Outline every malaria parasite.
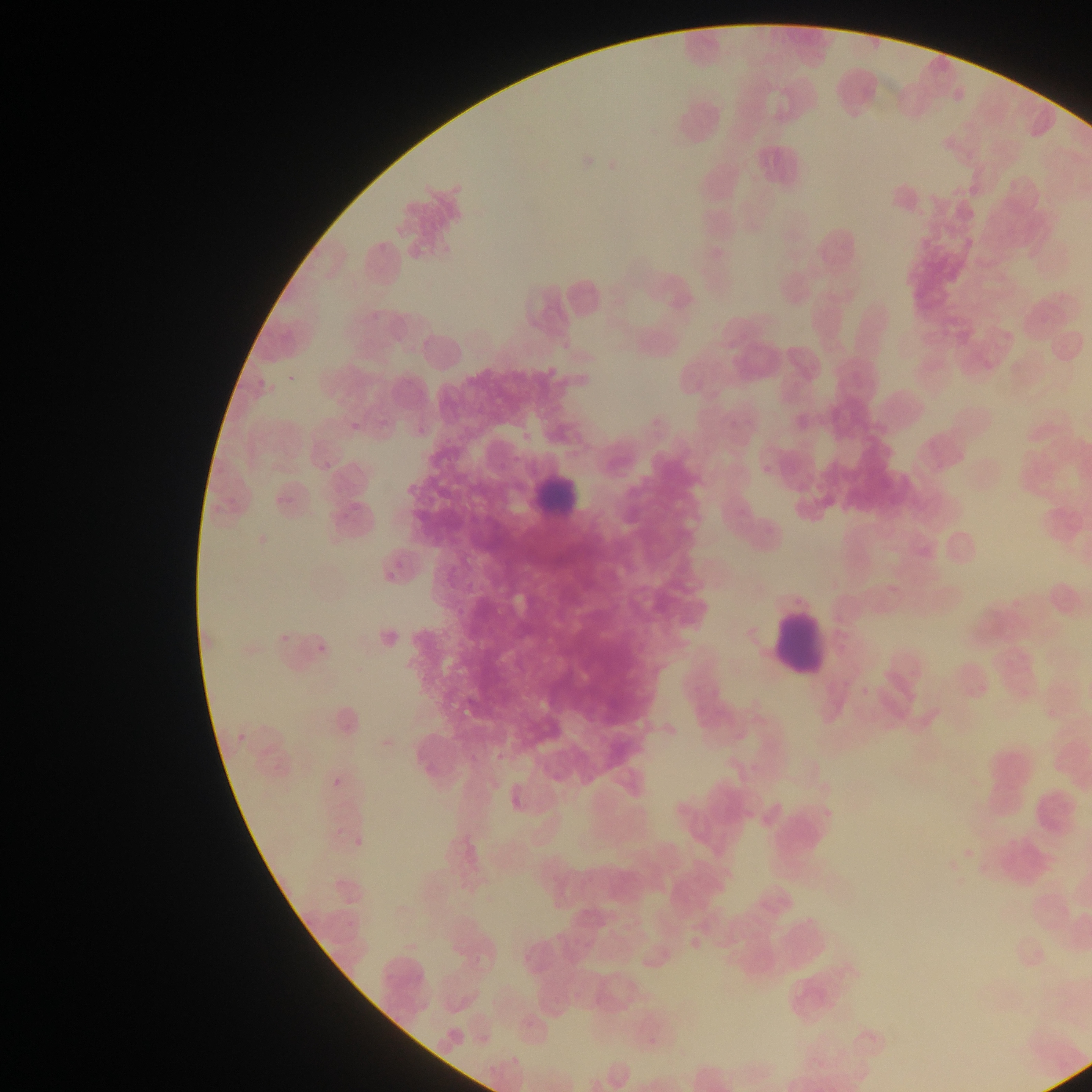
Approximate bounding boxes as [left, top, right, bottom] in pixels.
Malaria parasites: [307, 634, 341, 662], [321, 772, 349, 803], [351, 830, 377, 858].

capture = mobile-phone photograph through a microscope
leukocyte locations = approximate bounding boxes as [left, top, right, bottom] in pixels: [531, 463, 585, 523], [772, 611, 828, 676]
field of view = single
country = Ghana
preparation = thin blood smear
image size = 1092×1092 pixels